Report the malaria status of this cell.
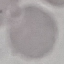
Uninfected.

Summary:
  - Capture: smartphone through the microscope eyepiece
  - Image type: cell patch, automatically extracted from a larger field of view and resized to 64 × 64 pixels
  - Preparation: thin blood smear
  - Stain: Giemsa